State which cell type is depicted.
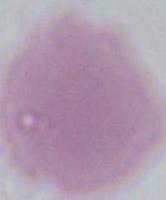

This is an erythrocyte.

Captured at 1000x magnification. Photomicrograph.